Classify this cell by malaria status.
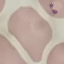
Parasitized.

Summary:
  - Preparation: thin smear
  - Capture: smartphone camera at the microscope eyepiece
  - Stain: Giemsa
  - Image type: automatically extracted cell patch, resized to 64 × 64 pixels